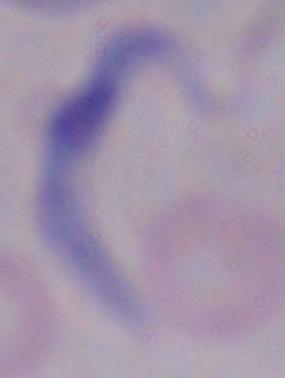

{
  "magnification": "1000x",
  "modality": "micrograph",
  "identification": "trypanosome"
}